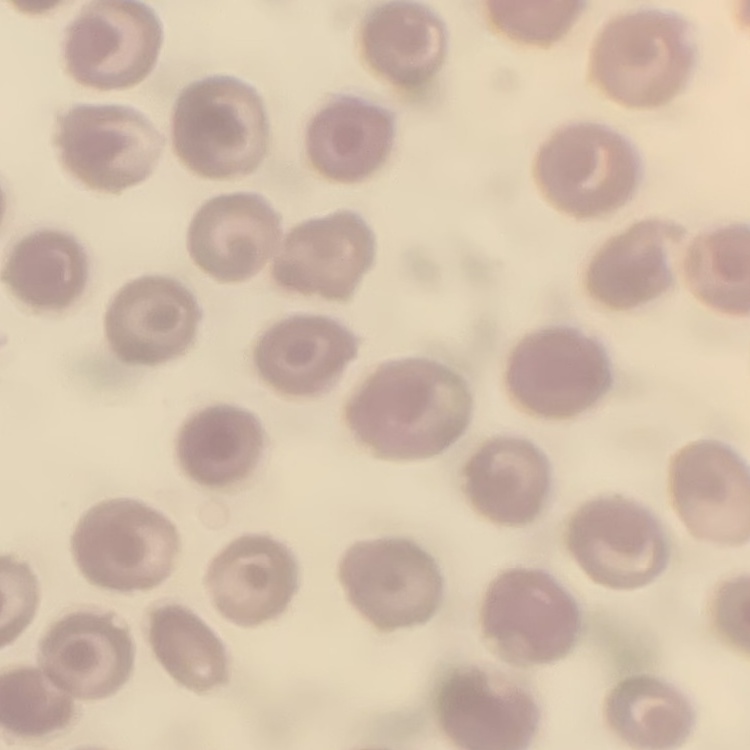
erythrocyte morphology = no rouleaux formation
preparation = thin blood film
stain = Field's or Giemsa
image type = square crop of a larger photomicrograph